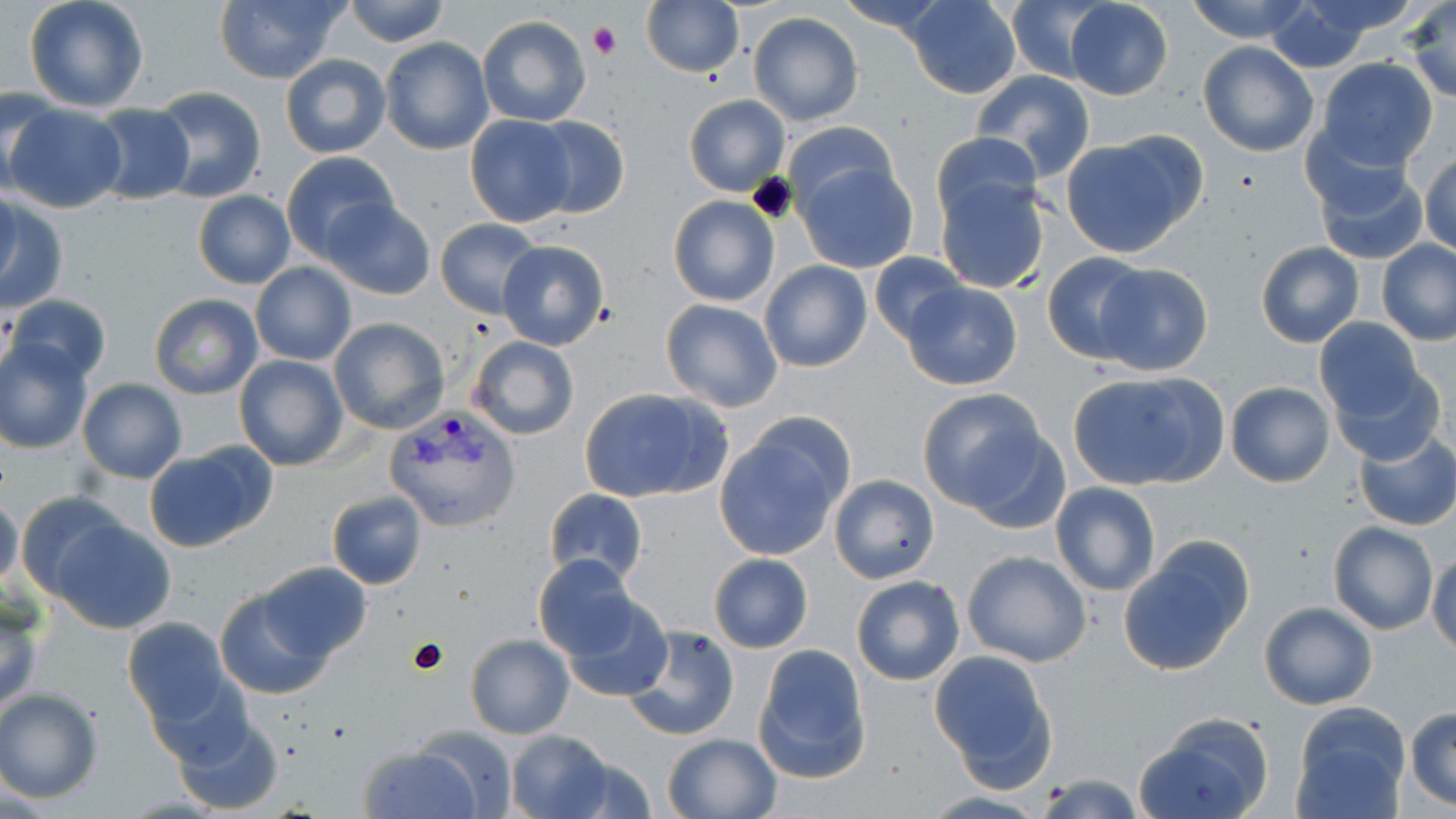
Approximate bounding boxes as (x1,y1)-(x2,y2) corner pairs in pixels. Platelet locations: (587,22)-(621,59). Plasmodium vivax-infected red blood cell locations: (382,405)-(522,534). Uninfected red blood cell locations: (24,0)-(150,113), (212,0)-(350,85), (340,0)-(452,47), (641,0)-(745,79), (834,0)-(954,33), (904,0)-(1022,98), (1183,0)-(1315,44), (1001,1)-(1109,84), (1405,1)-(1456,102), (1062,2)-(1173,100), (1264,3)-(1380,71), (748,11)-(863,126), (477,15)-(592,127), (379,36)-(493,155), (1198,41)-(1319,157), (280,54)-(391,158), (1316,57)-(1440,171), (970,71)-(1096,184), (148,87)-(268,204), (0,88)-(55,194), (684,94)-(790,195), (5,103)-(128,213), (87,105)-(195,204), (464,115)-(578,227), (529,115)-(630,219), (784,121)-(901,221), (930,131)-(1041,229), (1059,132)-(1204,258), (1420,150)-(1456,257), (279,151)-(400,261), (1311,154)-(1429,266), (795,159)-(918,275), (933,173)-(1051,294), (1,187)-(21,298), (192,191)-(295,289), (0,196)-(69,315), (667,196)-(778,308), (321,197)-(435,299), (435,218)-(543,317), (497,238)-(610,349), (1377,239)-(1456,345), (1255,241)-(1364,348), (1041,251)-(1151,364), (868,252)-(967,344), (758,260)-(872,372), (251,262)-(356,366), (1093,263)-(1214,377), (901,282)-(1022,390), (149,293)-(263,400), (8,294)-(110,386), (659,299)-(784,414), (328,317)-(450,434), (1313,317)-(1428,423), (466,335)-(580,441), (1,341)-(94,453), (234,355)-(350,471), (1328,363)-(1447,467), (1069,369)-(1230,489), (77,379)-(188,485), (1225,380)-(1335,487), (577,387)-(732,504), (917,393)-(1061,521), (715,421)-(851,561), (1354,430)-(1456,531), (144,441)-(275,551), (829,473)-(939,584), (1049,483)-(1161,597), (544,487)-(648,587), (17,491)-(136,607), (328,491)-(427,589), (0,492)-(24,594), (49,518)-(176,634), (1328,521)-(1438,635), (1118,541)-(1250,675), (1429,548)-(1456,654), (961,550)-(1092,666), (533,553)-(640,661), (708,555)-(813,654), (257,560)-(372,662), (851,577)-(965,685), (215,587)-(332,700), (556,596)-(672,703), (0,599)-(46,716), (1259,601)-(1376,710), (122,618)-(234,726), (623,625)-(741,741), (465,635)-(574,739), (752,645)-(873,783), (929,650)-(1059,790), (150,675)-(256,769), (0,688)-(104,803), (1289,702)-(1413,819), (1405,707)-(1456,811), (169,709)-(285,815), (1136,711)-(1275,819), (410,728)-(522,816), (506,729)-(617,818), (661,733)-(782,818), (357,743)-(483,819), (1034,774)-(1146,818). Slide-level diagnosis: Plasmodium vivax. Light microscopy. Captured at 1000x magnification. Thin blood smear. May-Grünwald-Giemsa-stained preparation. Image is 1456×819 pixels. One field of a larger specimen.